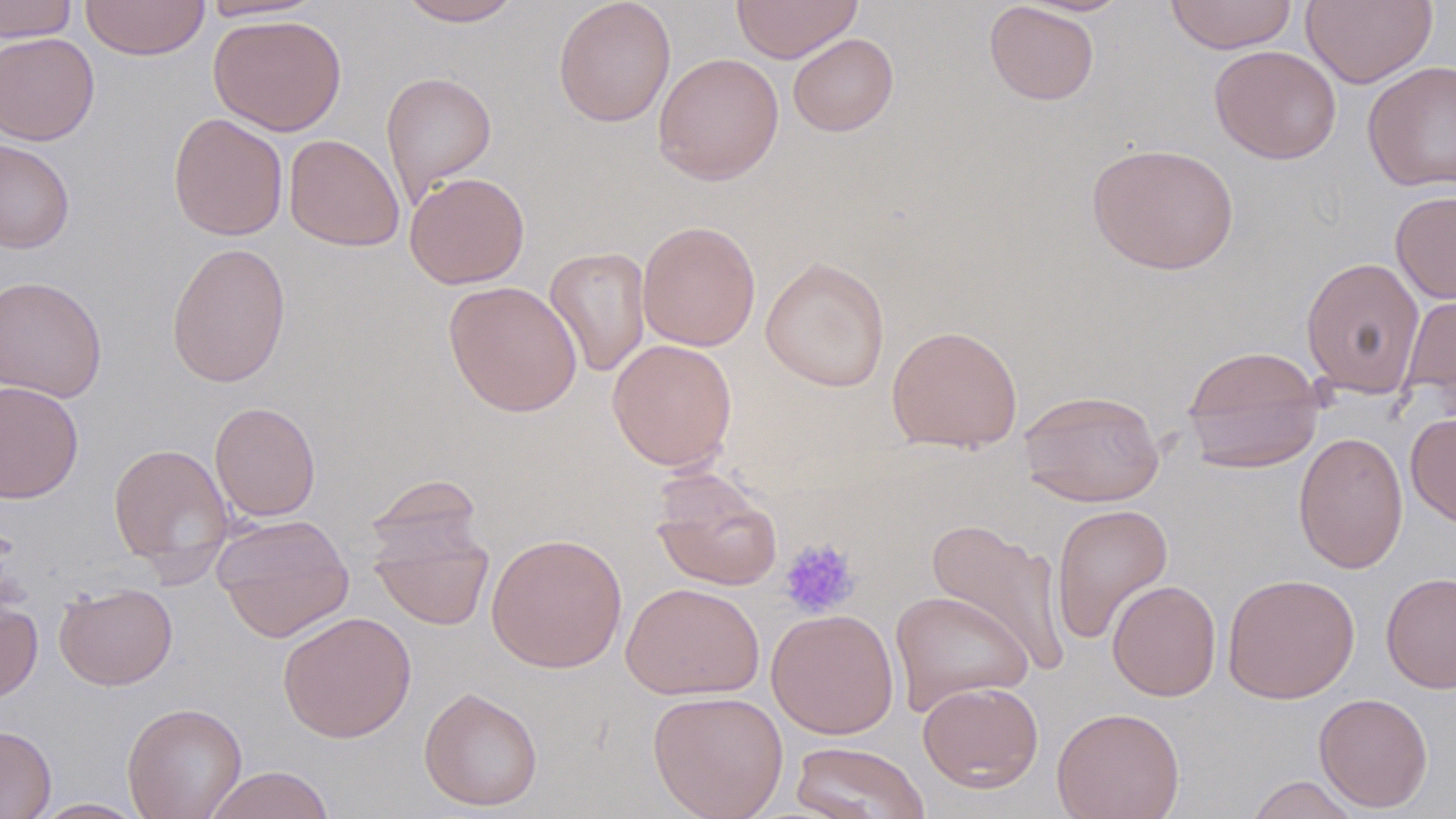

Summary:
  - Coordinate format: approximate bounding boxes as (x1, y1, x2, y2) in pixels
  - Uninfected red blood cell locations: (0, 0, 79, 42), (80, 0, 210, 60), (199, 0, 324, 21), (397, 0, 523, 26), (552, 0, 676, 128), (731, 0, 863, 63), (1164, 0, 1298, 54), (1301, 0, 1437, 89), (984, 1, 1100, 105), (208, 13, 347, 136), (0, 32, 99, 145), (787, 33, 899, 136), (1209, 44, 1342, 164), (652, 52, 784, 186), (1363, 61, 1456, 192), (380, 71, 497, 205), (168, 112, 288, 241), (284, 134, 404, 252), (0, 139, 75, 253), (1086, 142, 1240, 275), (404, 172, 530, 289), (1390, 190, 1456, 304), (637, 220, 761, 351), (166, 241, 292, 387), (544, 246, 652, 378), (1300, 256, 1425, 398), (760, 257, 890, 392), (0, 275, 108, 402), (443, 279, 582, 417), (1400, 289, 1456, 407), (886, 324, 1023, 453), (607, 339, 737, 472), (1181, 345, 1325, 473), (0, 380, 84, 504), (1017, 389, 1166, 507), (209, 401, 322, 522), (1405, 412, 1456, 528), (1293, 431, 1409, 575), (108, 442, 234, 576), (649, 469, 783, 591), (365, 473, 484, 566), (1050, 503, 1174, 645), (212, 514, 355, 643), (925, 517, 1070, 675), (369, 520, 494, 632), (486, 532, 627, 673), (1381, 571, 1456, 694), (1222, 572, 1360, 704), (1106, 579, 1222, 701), (53, 582, 178, 690), (621, 582, 764, 701), (890, 589, 1033, 716), (0, 595, 42, 705), (766, 608, 899, 739), (278, 611, 417, 743), (918, 680, 1044, 792), (418, 686, 543, 812), (647, 690, 789, 819), (1313, 692, 1433, 813), (122, 702, 247, 819), (1051, 707, 1185, 819), (0, 724, 56, 819), (790, 741, 930, 819), (204, 765, 335, 819), (1245, 774, 1363, 819), (29, 798, 150, 818)
  - Platelet locations: (778, 537, 861, 619)
  - Slide-level diagnosis: no evidence of blood parasites
  - Preparation: thin blood film
  - Image size: 1456×819 pixels
  - Stain: May-Grünwald-Giemsa
  - Field of view: one of a larger specimen
  - Magnification: 1000x
  - Modality: light microscopy